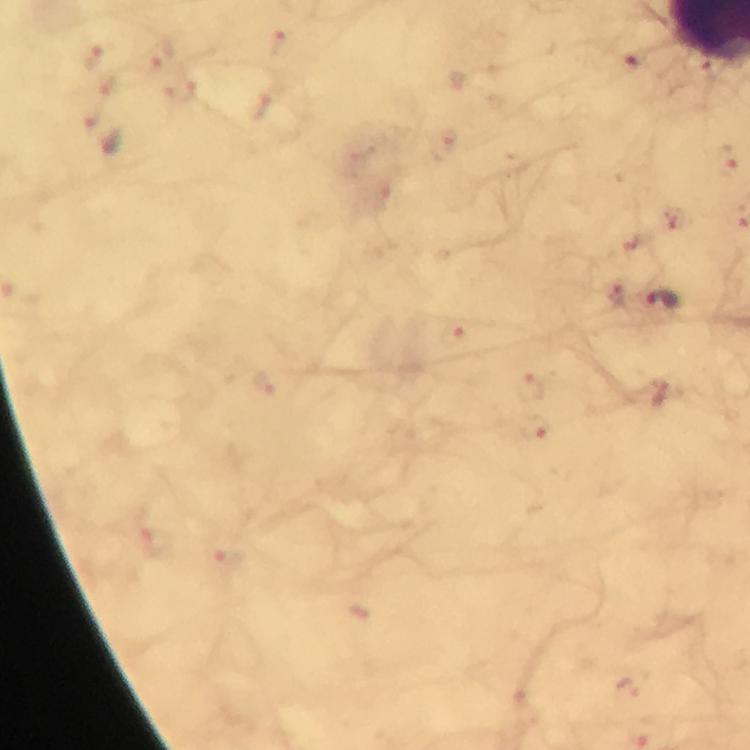

Approximate centers as (x, y) in pixels.
Summary:
  - Plasmodium parasite locations: (281, 44), (92, 56), (161, 56), (635, 61), (109, 84), (262, 106), (91, 112), (723, 163), (675, 215), (617, 299), (664, 301), (454, 334), (267, 383), (532, 387), (539, 430), (159, 542), (226, 561), (636, 683)
  - Context: from a diagnostic examination for malaria
  - Stain: Giemsa
  - Capture: smartphone camera through the microscope
  - Cropped from: a single field of view
  - Magnification: 100x
  - Image size: 750×750 pixels
  - Immersion oil: used
  - Preparation: thick blood film